Assess the morphology of the red blood cells.
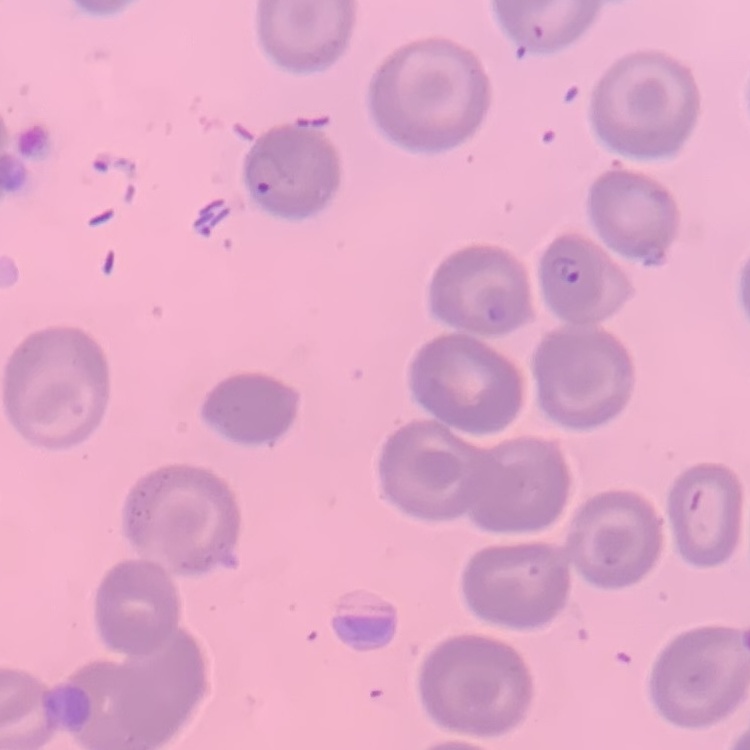
No rouleaux formation.

Summary:
  - Preparation: thin blood film
  - Image type: square crop of a larger photomicrograph
  - Stain: Field's or Giemsa